Comment on the morphology of the red blood cells.
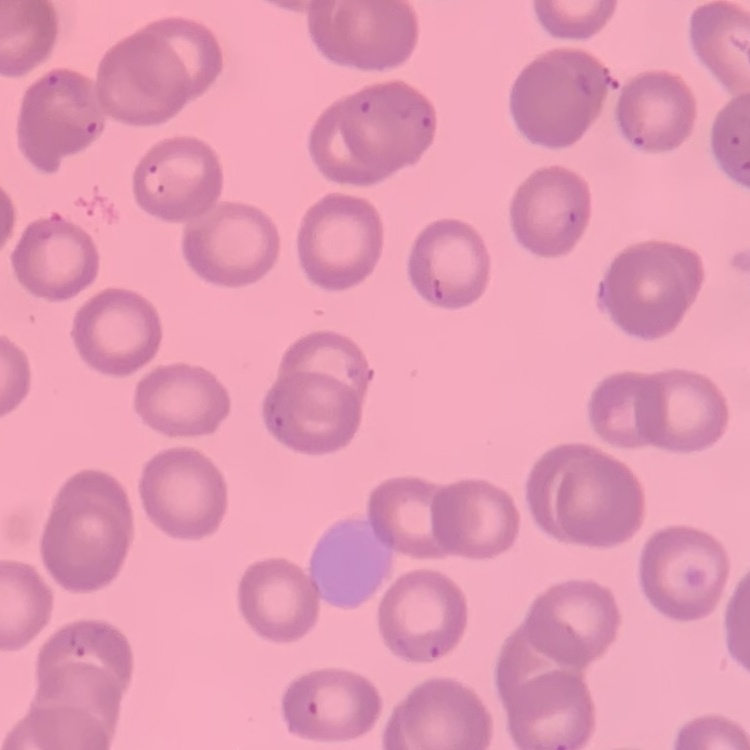
They show no rouleaux formation.

image_type: square crop of a larger photomicrograph
stain: Field's or Giemsa
preparation: thin blood smear